Assess this cell for malaria.
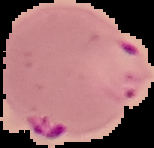

Parasitized.

Summary:
  - Image type: segmented cell region on a black background
  - Image size: 154×148 pixels
  - Preparation: thin blood smear